Outline each uninfected red blood cell.
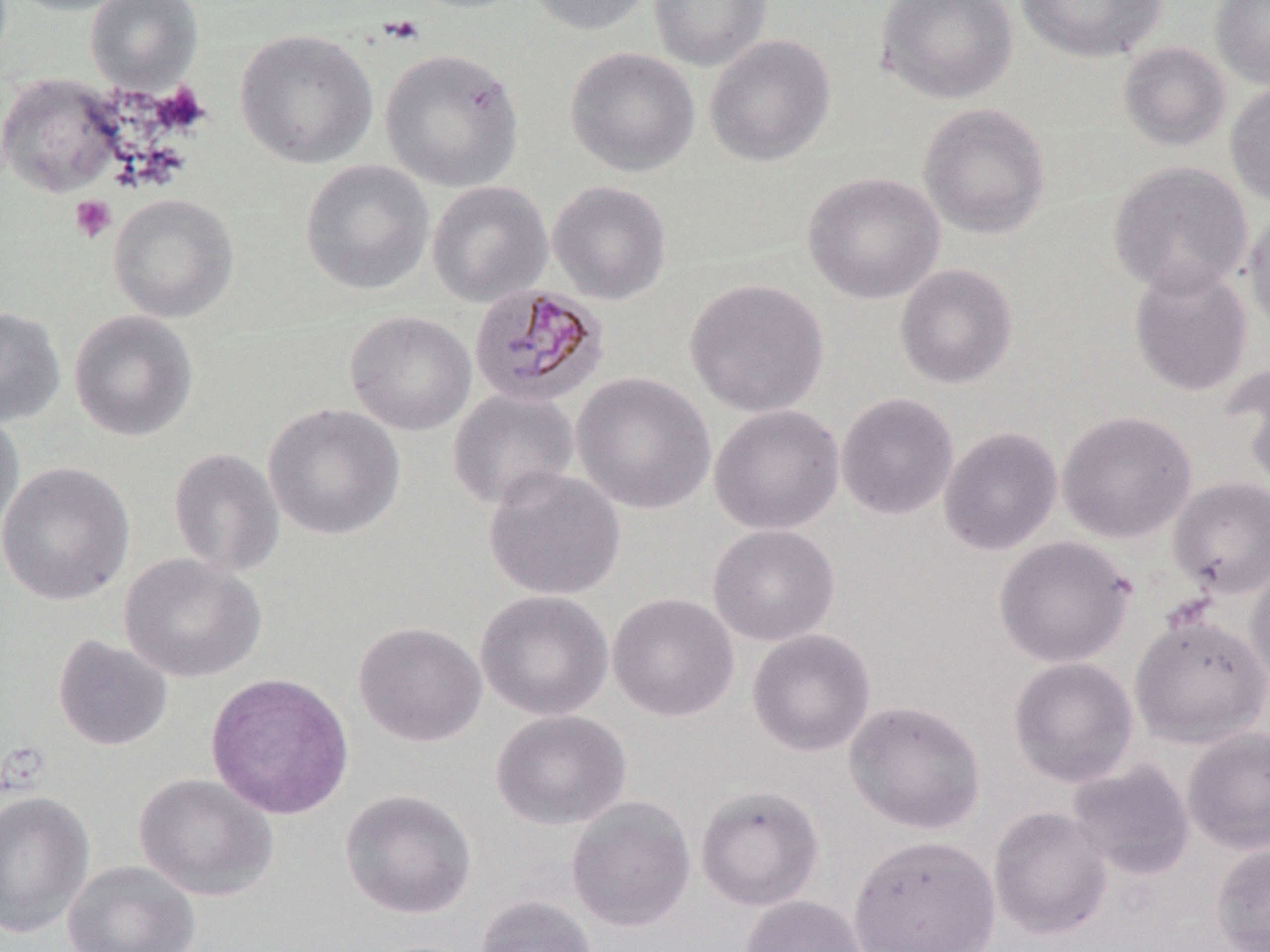

Approximate bounding boxes as (x1,y1)-(x2,y2) corner pairs in pixels.
Uninfected red blood cells: (3,0)-(137,16), (85,0)-(203,92), (525,0)-(653,36), (649,0)-(773,72), (875,0)-(1018,105), (1015,0)-(1168,63), (1210,0)-(1270,88), (235,28)-(378,169), (704,34)-(835,167), (1118,42)-(1230,152), (565,46)-(700,177), (379,48)-(525,192), (1,72)-(124,198), (1225,80)-(1270,208), (918,102)-(1051,239), (301,159)-(435,295), (1108,161)-(1253,298), (803,171)-(945,304), (427,180)-(553,306), (547,180)-(671,305), (108,193)-(238,323), (1243,205)-(1270,338), (1128,262)-(1253,397), (894,263)-(1018,389), (685,278)-(829,418), (0,306)-(66,427), (69,310)-(198,443), (345,310)-(476,436), (1224,363)-(1270,492), (571,372)-(716,515), (447,388)-(579,511), (836,392)-(959,521), (262,403)-(405,540), (709,404)-(844,535), (0,410)-(25,547), (1057,410)-(1196,543), (938,426)-(1062,556), (168,447)-(285,578), (0,461)-(135,606), (483,466)-(626,601), (1167,477)-(1270,598), (707,524)-(840,646), (994,535)-(1135,668), (119,553)-(266,683), (1246,558)-(1270,690), (475,590)-(614,721), (607,592)-(739,722), (1130,614)-(1270,747), (353,621)-(487,747), (747,628)-(876,757), (52,634)-(173,751), (1008,656)-(1139,788), (206,672)-(354,820), (844,699)-(986,834), (490,710)-(631,831), (1181,726)-(1270,854), (1066,758)-(1195,881), (133,772)-(279,901), (695,784)-(824,912), (339,788)-(477,920), (0,790)-(95,938), (565,796)-(696,932), (988,806)-(1113,939), (848,834)-(1001,952), (1210,841)-(1270,952), (62,860)-(201,952), (475,894)-(599,952), (739,894)-(869,952).

Plasmodium malariae-infected red blood cell locations: (469,284)-(607,408). Platelet locations: (378,15)-(425,45), (70,195)-(116,243). Slide-level diagnosis: Plasmodium malariae. Thin blood film. Light microscopy. One field of a larger specimen. Captured at 1000x magnification. May-Grünwald-Giemsa-stained preparation. Image is 1270×952 pixels.